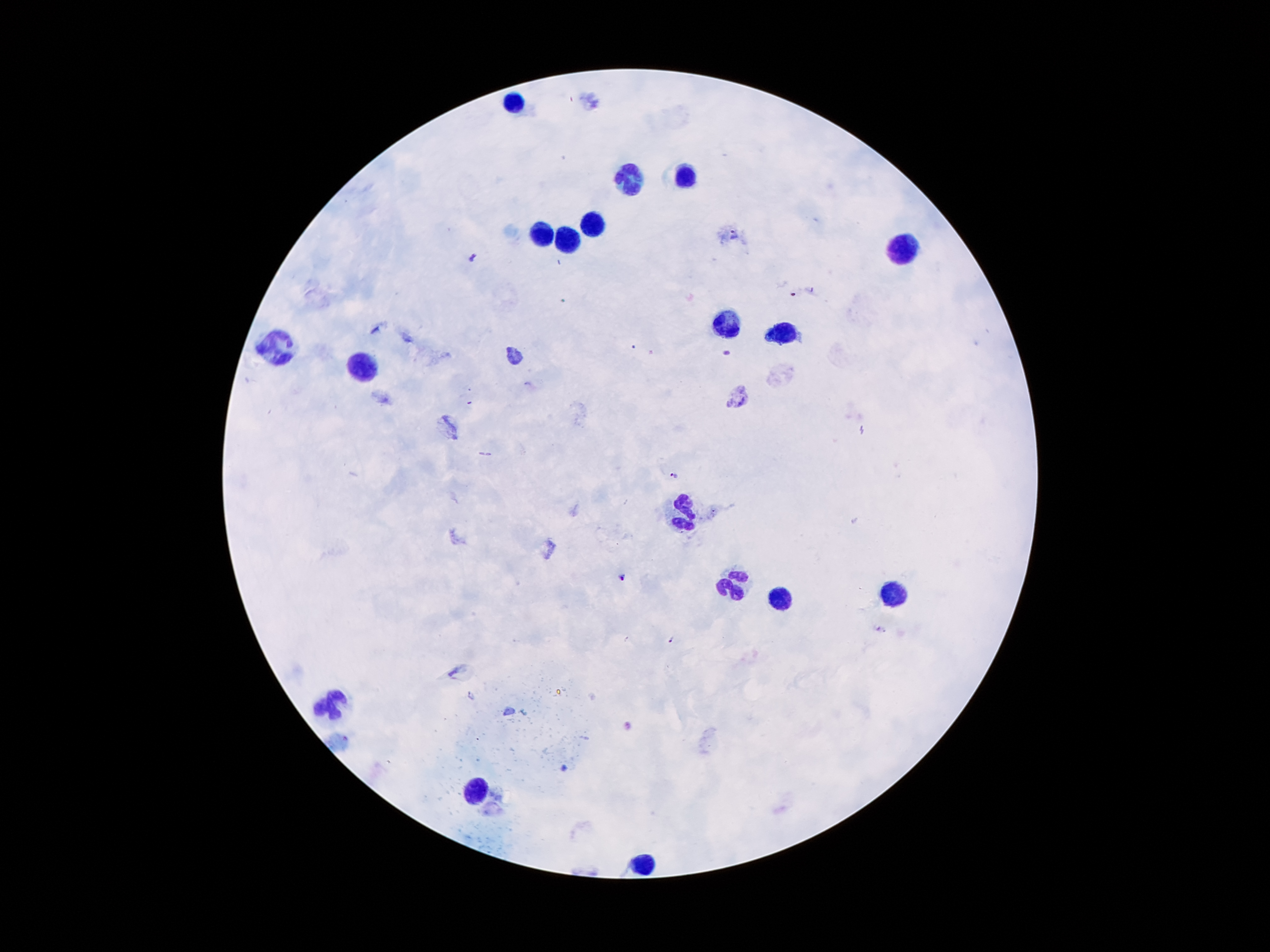

Patient malaria status: positive for Plasmodium falciparum. 100x magnification. Photographed through the microscope eyepiece with a smartphone camera. Thick blood film. Image is 1270×952 pixels. Giemsa-stained preparation. One field from this slide.